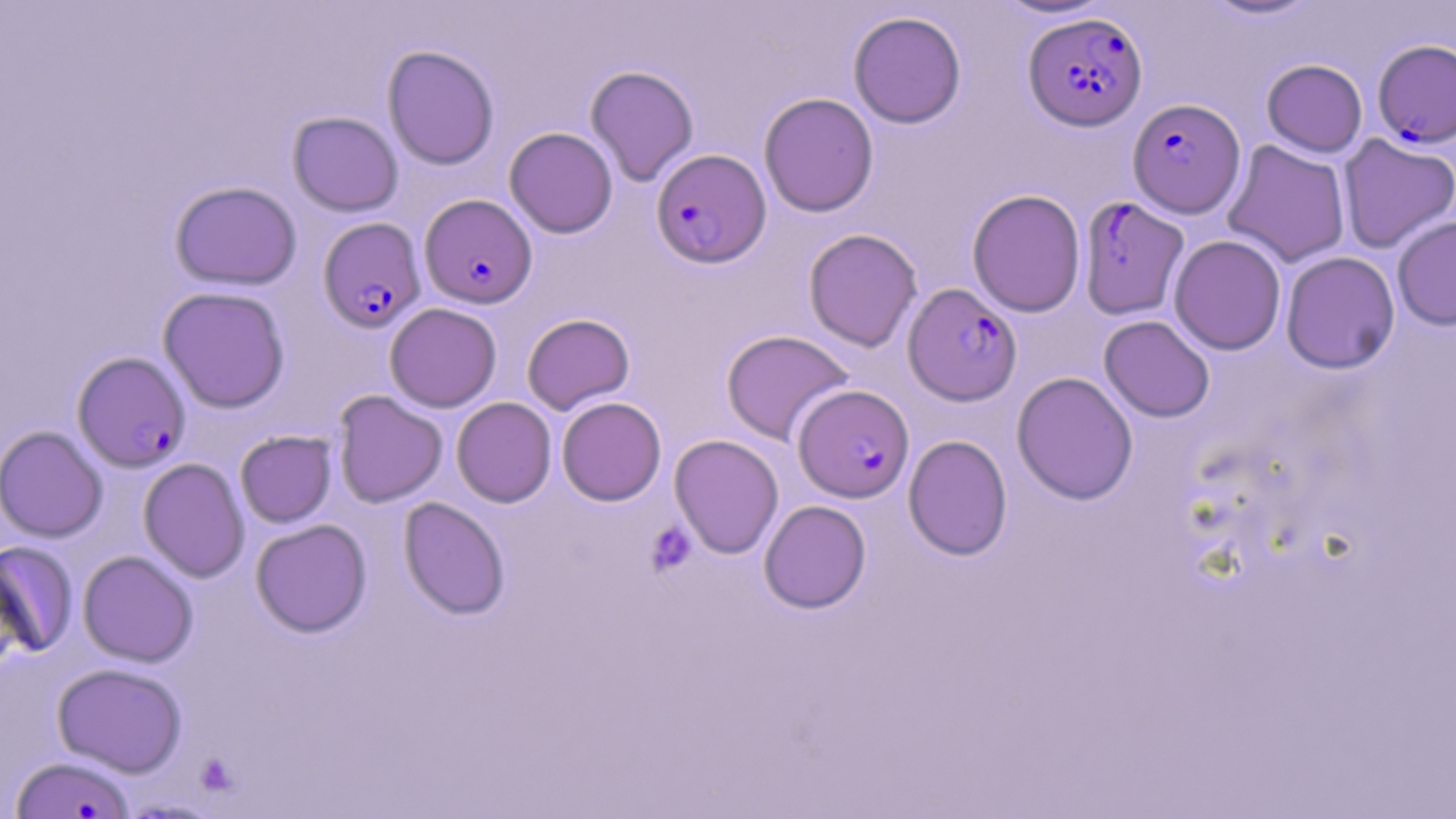

Approximate bounding boxes as named x1/y1/x2/y2 corners in pixels. Uninfected red blood cell locations: (x1=991, y1=0, x2=1116, y2=20), (x1=1199, y1=0, x2=1323, y2=21), (x1=848, y1=10, x2=966, y2=128), (x1=382, y1=45, x2=499, y2=169), (x1=1261, y1=59, x2=1367, y2=157), (x1=585, y1=65, x2=699, y2=186), (x1=759, y1=92, x2=879, y2=217), (x1=287, y1=111, x2=403, y2=216), (x1=504, y1=127, x2=618, y2=238), (x1=1337, y1=134, x2=1456, y2=254), (x1=1222, y1=140, x2=1351, y2=267), (x1=169, y1=181, x2=302, y2=290), (x1=967, y1=189, x2=1086, y2=317), (x1=1392, y1=215, x2=1456, y2=330), (x1=804, y1=228, x2=922, y2=352), (x1=1169, y1=235, x2=1286, y2=355), (x1=1280, y1=251, x2=1400, y2=373), (x1=158, y1=286, x2=290, y2=413), (x1=384, y1=302, x2=502, y2=412), (x1=522, y1=313, x2=634, y2=414), (x1=1099, y1=315, x2=1215, y2=422), (x1=721, y1=329, x2=854, y2=446), (x1=1011, y1=372, x2=1139, y2=505), (x1=332, y1=390, x2=448, y2=507), (x1=556, y1=396, x2=666, y2=506), (x1=452, y1=397, x2=556, y2=507), (x1=0, y1=425, x2=108, y2=542), (x1=235, y1=431, x2=337, y2=527), (x1=669, y1=434, x2=784, y2=559), (x1=903, y1=435, x2=1012, y2=560), (x1=138, y1=458, x2=250, y2=582), (x1=399, y1=497, x2=510, y2=619), (x1=759, y1=500, x2=871, y2=613), (x1=250, y1=518, x2=372, y2=637), (x1=1, y1=541, x2=79, y2=658), (x1=78, y1=550, x2=198, y2=667), (x1=52, y1=663, x2=187, y2=776). Platelet locations: (x1=646, y1=522, x2=697, y2=575). Plasmodium falciparum-infected red blood cell locations: (x1=1024, y1=12, x2=1147, y2=130), (x1=1373, y1=39, x2=1456, y2=147), (x1=1127, y1=98, x2=1245, y2=218), (x1=651, y1=150, x2=771, y2=267), (x1=420, y1=193, x2=537, y2=309), (x1=1077, y1=196, x2=1189, y2=318), (x1=319, y1=217, x2=427, y2=333), (x1=903, y1=283, x2=1021, y2=405), (x1=73, y1=351, x2=191, y2=472), (x1=793, y1=384, x2=914, y2=502), (x1=11, y1=755, x2=136, y2=819). Slide-level diagnosis: Plasmodium falciparum. May-Grünwald-Giemsa stain. Thin blood smear. Image is 1456×819 pixels. Single field of view. Captured at 1000x magnification. Optical microscopy.